Classify this cell by malaria status.
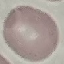
It is uninfected.

{
  "preparation": "thin smear",
  "capture": "smartphone camera at the microscope eyepiece",
  "stain": "Giemsa",
  "image_type": "automatically extracted cell patch, resized to 64 × 64 pixels"
}